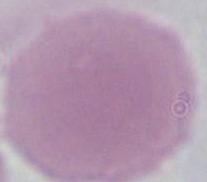
{
  "modality": "micrograph",
  "magnification": "1000x",
  "identification": "red blood cell"
}